Point out each malaria parasite and each leukocyte.
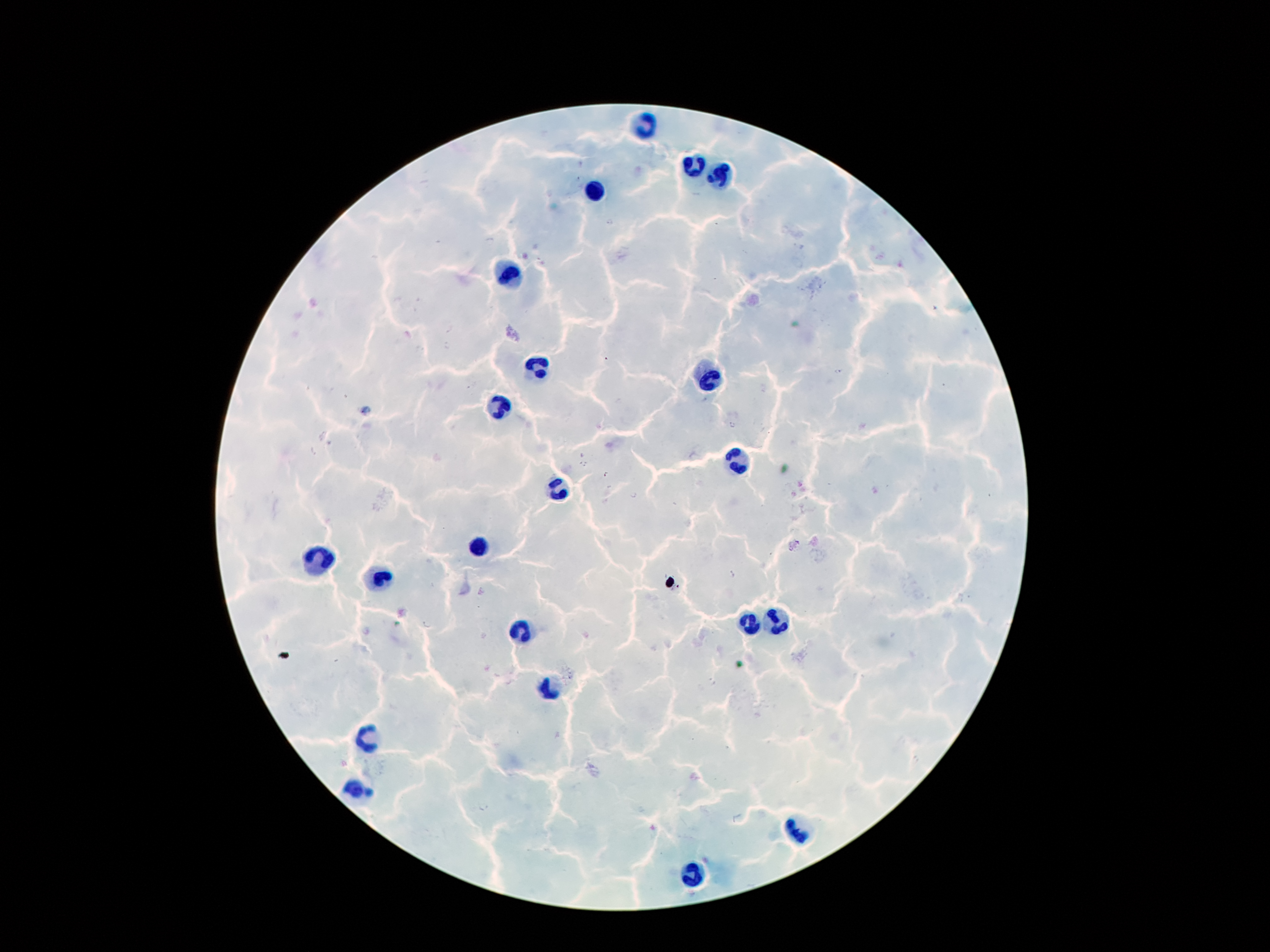

Approximate centers as [x, y] in pixels.
Malaria parasites: [575, 178], [609, 223], [489, 241], [450, 329], [446, 345], [607, 359], [838, 372], [733, 426], [312, 451], [583, 465], [606, 474], [634, 495], [733, 575], [428, 623], [713, 683], [483, 808].
Leukocytes: [640, 121], [691, 165], [721, 174], [593, 193], [512, 274], [539, 363], [709, 380], [500, 410], [735, 463], [561, 491], [479, 548], [315, 557], [381, 580], [749, 620], [777, 620], [521, 629], [549, 688], [369, 737], [355, 790], [798, 828], [689, 876].

Smartphone photograph taken through the microscope eyepiece. One field from this slide. Thick peripheral-blood smear. Image is 1270×952 pixels. Patient malaria status: infected with Plasmodium falciparum. 100x magnification. Giemsa-stained preparation.